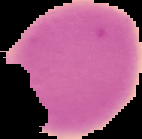
From a thin blood smear. Malaria status: uninfected. Image is 142×139 pixels. Cell region segmented out of the field of view; the surrounding area is masked to black.